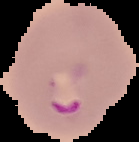
Image is 139×142 pixels. From a thin blood film. Result: Plasmodium parasites detected. Segmented cell region on a black background.